Assess this cell for malaria.
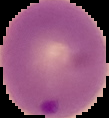

It is parasitized.

From a thin blood smear. The area outside the segmented cell region is set to black. Image is 109×118 pixels.